Evaluate for malaria.
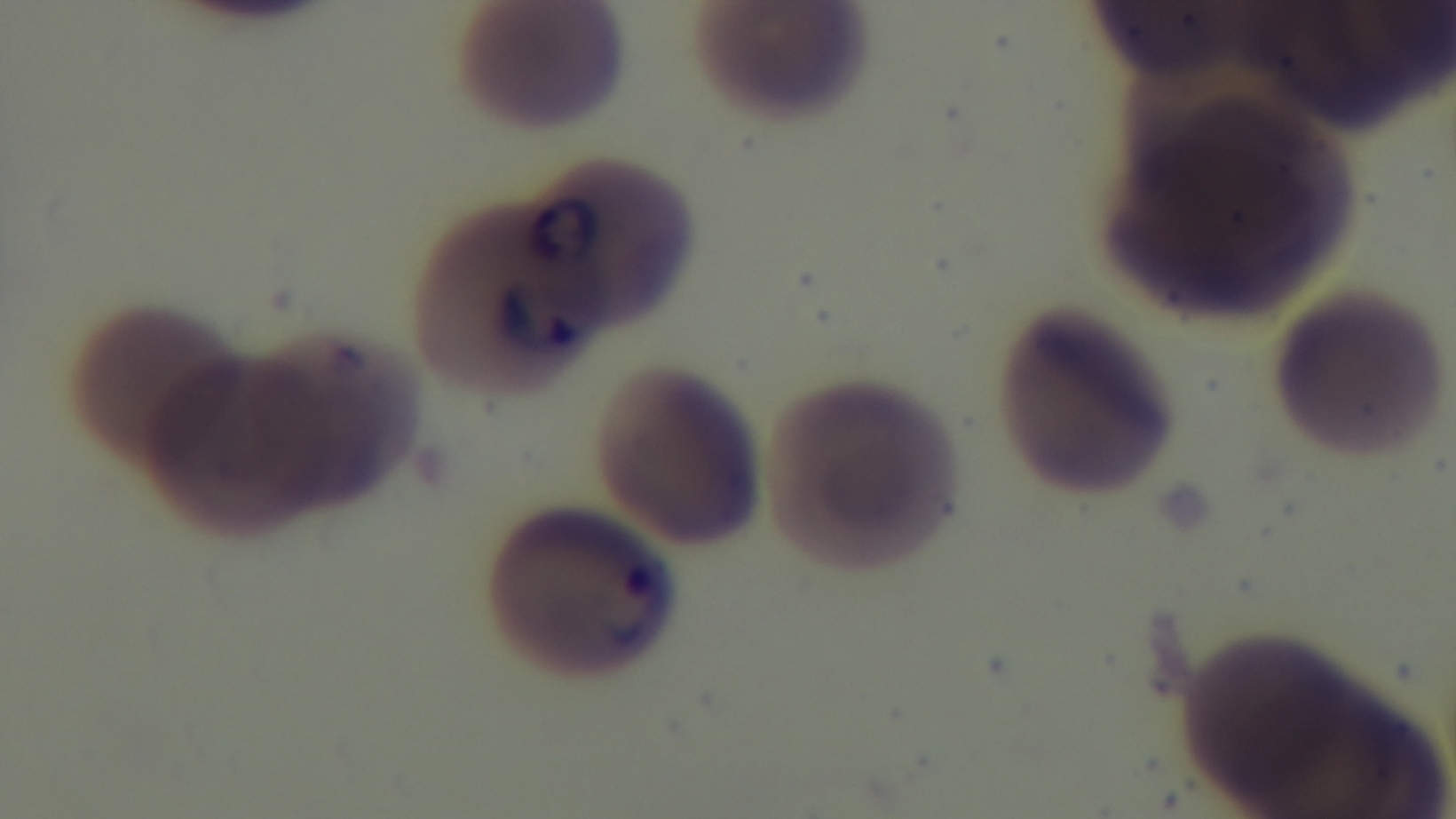
Infected.

Summary:
  - Stain: Giemsa
  - Capture: mounted 4K digital camera
  - Field of view: single
  - Preparation: thin blood film
  - Modality: light microscopy
  - Objective: 100x oil immersion